Evaluate for Plasmodium parasites.
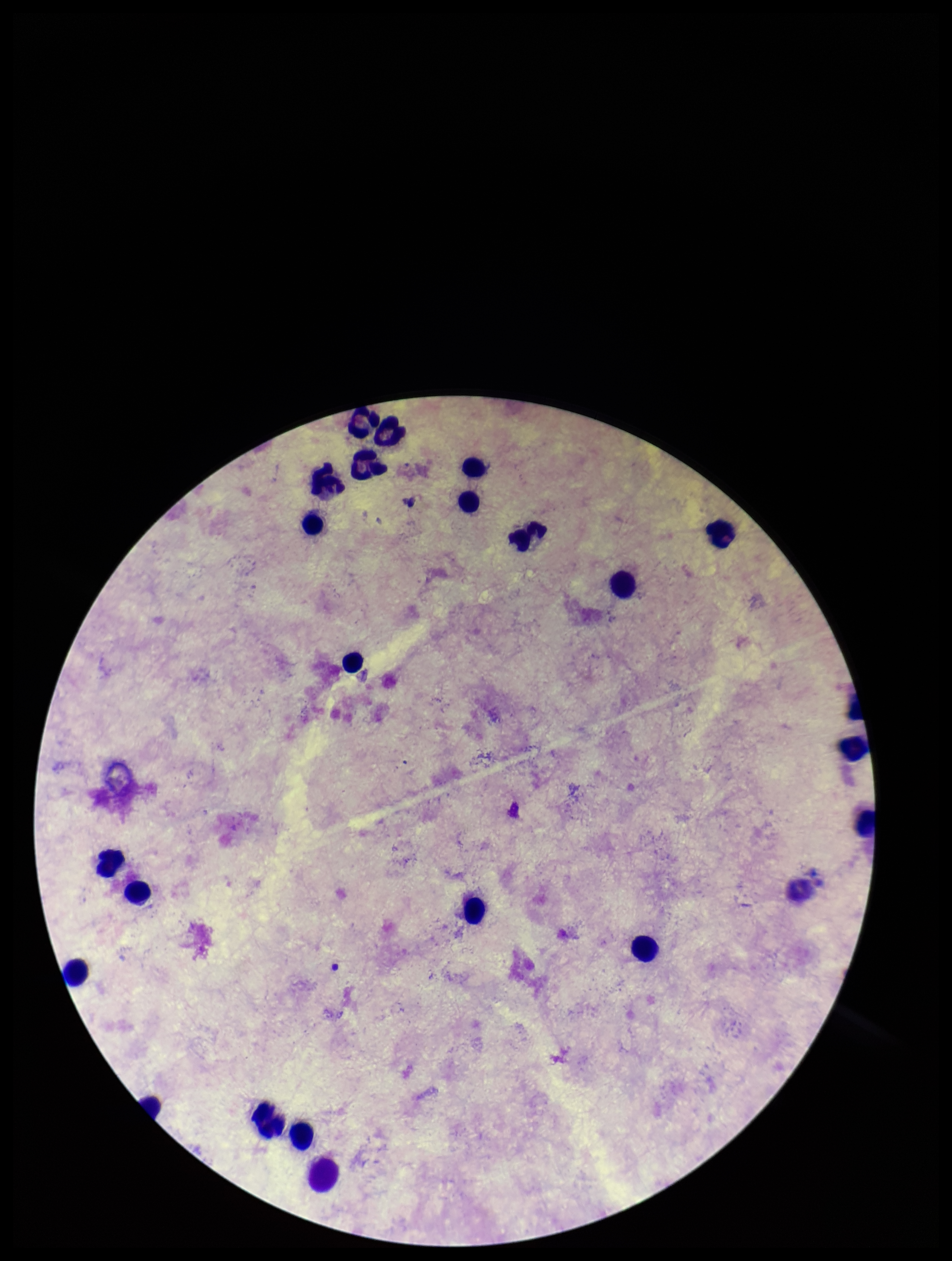

None detected.

{
  "patient_malaria_status": "negative",
  "preparation": "thick blood smear",
  "image_size": "952×1261 pixels",
  "capture": "smartphone photograph through the microscope eyepiece",
  "stain": "Giemsa",
  "parasite_count": 0,
  "field_of_view": "single",
  "leukocyte_count": 23
}